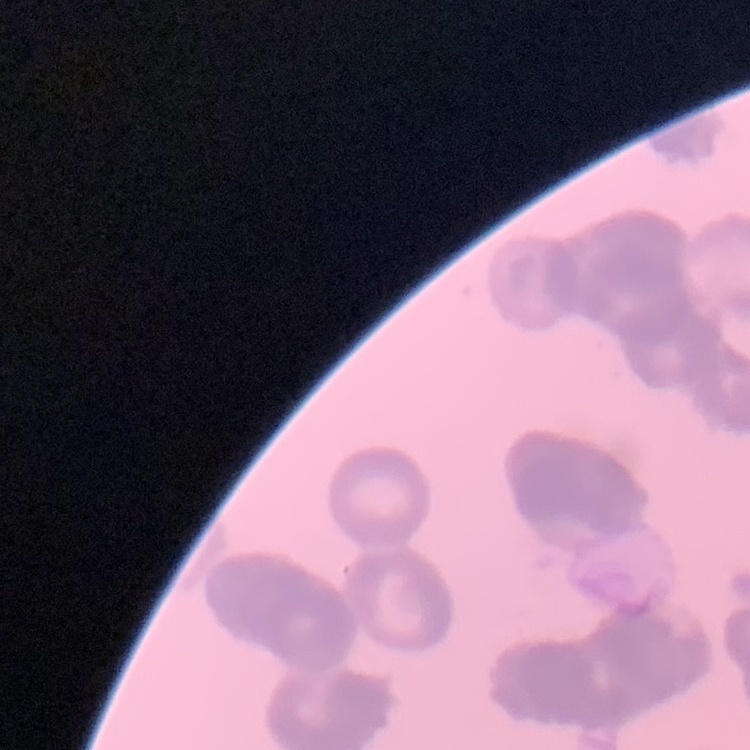

The erythrocytes exhibit rouleaux formation. Square crop of a larger photomicrograph. Thin blood film. Field's or Giemsa stain.